Describe the morphology of the erythrocytes.
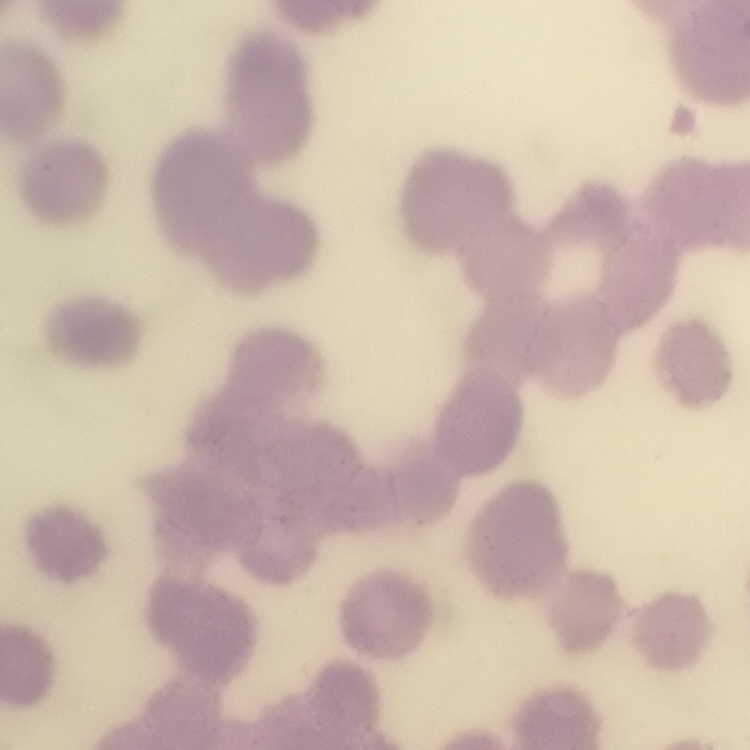

They show rouleaux formation.

stain = Field's or Giemsa
image type = one tile cut from a larger photomicrograph
preparation = thin blood smear